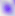

Captured at 400x magnification. Toxoplasma gondii is shown. Micrograph.